Assess the morphology of the erythrocytes.
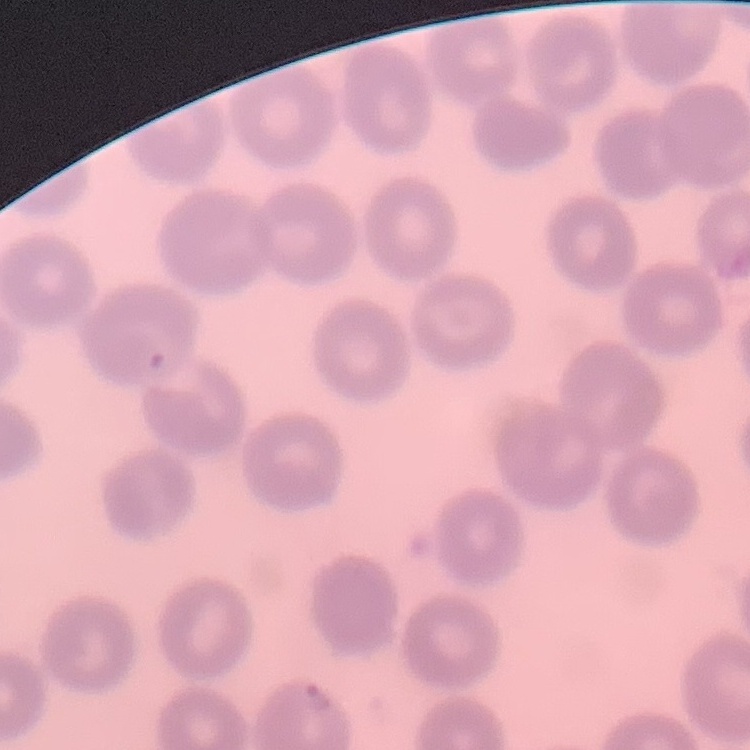

No rouleaux formation.

Field's or Giemsa stain. Thin blood smear. Square crop of a larger photomicrograph.